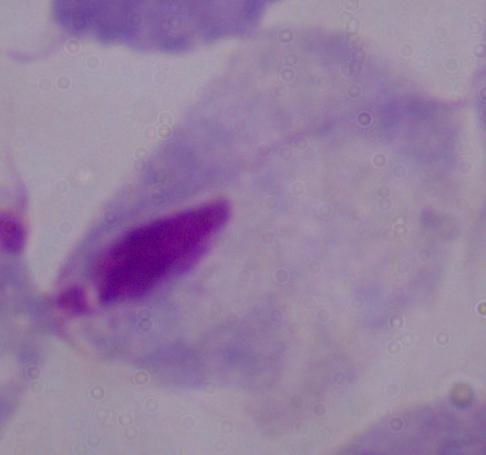

Summary:
  - Magnification: 1000x
  - Identification: trichomonad
  - Modality: photomicrograph